Locate every blood parasite and identify its species.
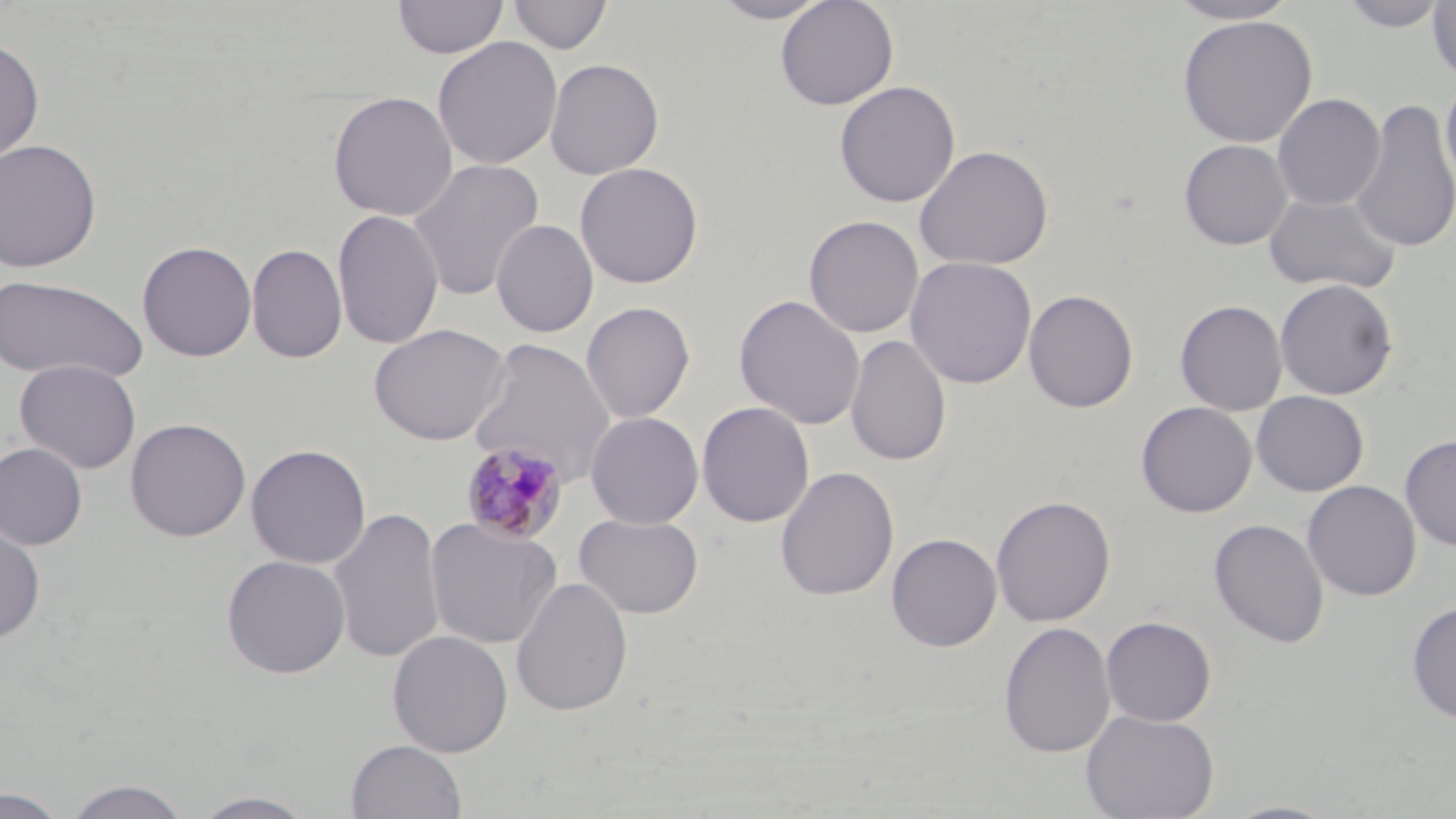

Approximate bounding boxes as [x1, y1, x2, y2] in pixels.
Plasmodium malariae-infected red blood cells: [460, 440, 569, 545].
No Plasmodium falciparum, Plasmodium ovale, Plasmodium vivax, Babesia divergens, or Trypanosoma brucei observed.

Uninfected red blood cell locations: [393, 0, 508, 59], [507, 0, 613, 55], [710, 0, 833, 23], [775, 0, 899, 110], [1165, 0, 1304, 25], [1338, 0, 1449, 32], [1427, 0, 1456, 84], [1177, 15, 1318, 147], [432, 36, 563, 170], [0, 37, 45, 165], [544, 58, 664, 180], [1440, 72, 1456, 196], [834, 80, 960, 208], [328, 91, 458, 221], [1272, 93, 1385, 211], [1348, 97, 1456, 255], [0, 138, 102, 273], [1179, 139, 1292, 250], [914, 144, 1054, 270], [407, 158, 545, 301], [575, 162, 704, 289], [1264, 190, 1400, 295], [332, 209, 444, 350], [804, 215, 924, 338], [491, 219, 599, 337], [137, 240, 257, 361], [246, 243, 347, 363], [905, 256, 1037, 389], [0, 275, 150, 385], [1274, 278, 1398, 400], [1024, 289, 1138, 413], [734, 293, 865, 430], [1175, 300, 1287, 415], [580, 301, 695, 424], [368, 323, 511, 446], [845, 333, 952, 468], [466, 338, 617, 488], [14, 358, 141, 474], [1251, 390, 1369, 496], [697, 401, 815, 528], [1136, 401, 1257, 517], [586, 411, 704, 528], [124, 417, 251, 542], [1400, 435, 1456, 552], [0, 442, 88, 550], [245, 443, 371, 569], [775, 465, 900, 602], [1303, 480, 1421, 601], [991, 494, 1116, 627], [328, 505, 445, 665], [573, 512, 704, 619], [425, 516, 563, 651], [0, 517, 46, 645], [1209, 518, 1330, 649], [887, 533, 1002, 652], [221, 554, 351, 679], [511, 575, 634, 717], [1406, 601, 1456, 725], [1101, 615, 1217, 726], [998, 620, 1116, 758], [387, 630, 514, 758], [1081, 708, 1219, 819], [345, 738, 467, 819], [61, 778, 192, 819], [1, 787, 70, 818], [189, 791, 321, 818], [1221, 800, 1343, 819]. Slide-level diagnosis: Plasmodium malariae. May-Grünwald-Giemsa stain. Thin blood smear. Optical microscopy. Captured at 1000x magnification. Image is 1456×819 pixels. One field of a larger specimen.